Give the position of every malaria parasite.
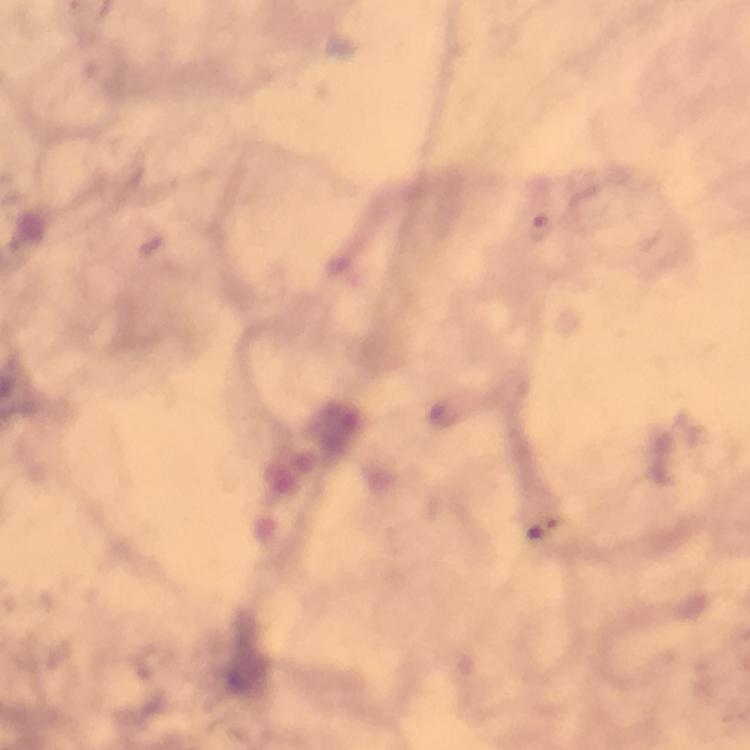

Approximate object centers, in pixels from the top-left corner.
Malaria parasites: (x=539, y=229).

stain = Giemsa
image size = 750×750 pixels
capture = smartphone camera through the microscope
context = from a malaria diagnostic workup
preparation = thick blood film
immersion oil = applied
magnification = 100x
cropped from = a single field of view